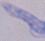
modality = photomicrograph
magnification = 1000x
identification = trypanosome